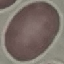
Summary:
  - Malaria status: uninfected
  - Preparation: thin blood smear
  - Capture: smartphone camera at the microscope eyepiece
  - Image type: automatically extracted cell patch, resized to 64 × 64 pixels
  - Stain: Giemsa